Point out each Plasmodium parasite.
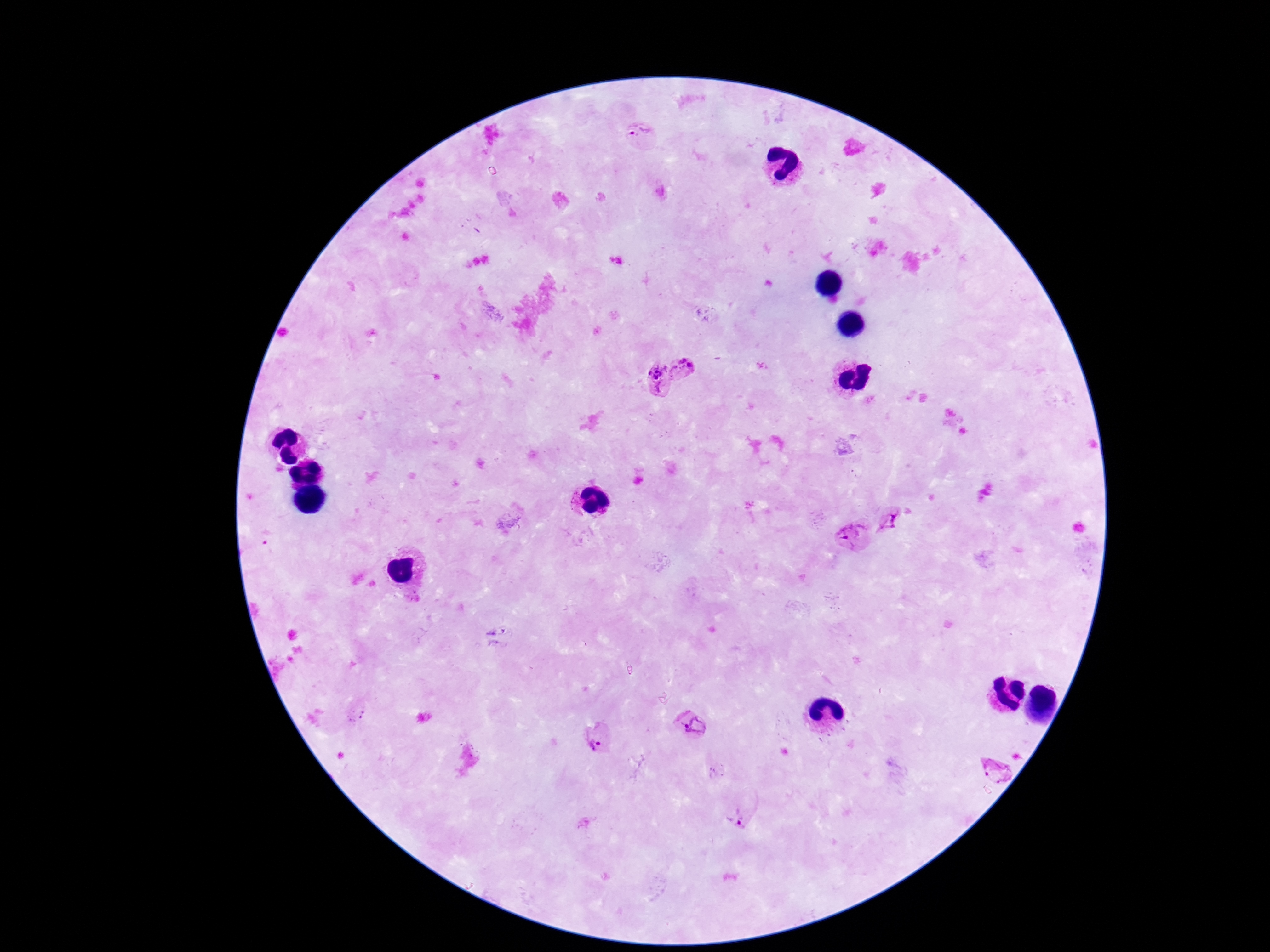

Approximate centers as [x, y] in pixels.
Plasmodium parasites: [641, 133], [685, 369], [655, 379], [891, 520], [850, 537], [692, 728], [598, 735], [998, 771], [740, 815].

100x magnification. Smartphone photograph taken through the microscope eyepiece. Giemsa stain. One field from this slide. Patient malaria status: infected. Image is 1270×952 pixels. Thick peripheral-blood smear.